State which parasite is depicted.
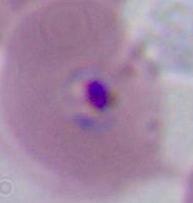

Plasmodium.

Summary:
  - Magnification: 400x or 1000x
  - Modality: micrograph